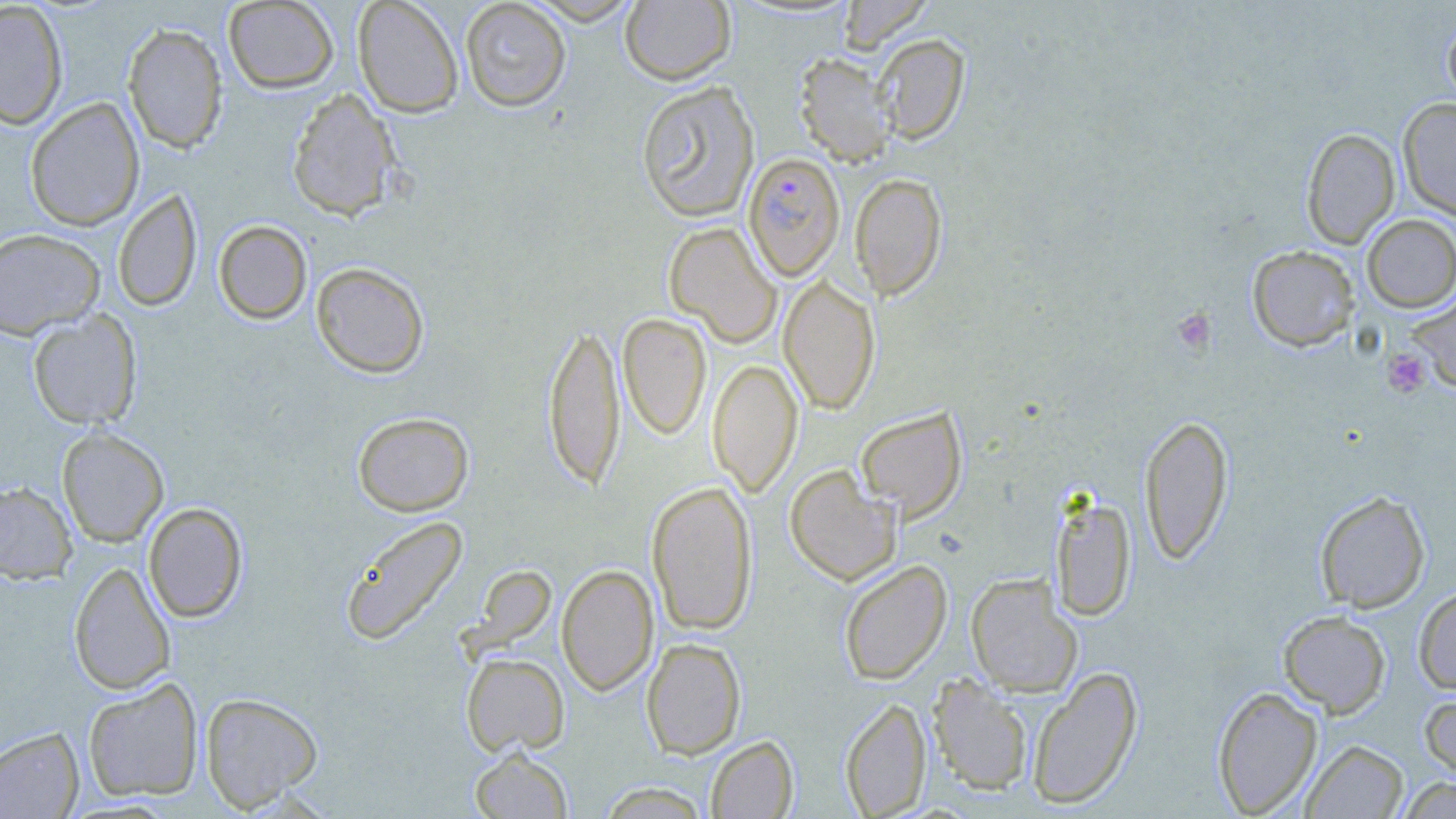

Summary:
  - Coordinate format: approximate bounding boxes as [x1, y1, x2, y2] in pixels
  - Uninfected red blood cell locations: [223, 0, 339, 93], [352, 0, 464, 118], [459, 0, 572, 112], [526, 0, 644, 25], [620, 0, 736, 85], [837, 0, 933, 55], [0, 2, 69, 130], [1442, 13, 1456, 112], [122, 22, 228, 154], [873, 33, 969, 143], [793, 53, 896, 166], [636, 80, 761, 222], [286, 88, 401, 221], [25, 97, 145, 231], [1398, 98, 1456, 220], [1301, 128, 1400, 248], [850, 173, 947, 300], [112, 189, 202, 312], [1361, 214, 1456, 312], [214, 220, 312, 324], [664, 222, 781, 347], [0, 228, 105, 339], [1246, 245, 1359, 351], [311, 262, 430, 378], [779, 274, 880, 414], [1405, 291, 1456, 393], [27, 310, 143, 429], [618, 313, 712, 440], [543, 319, 625, 491], [708, 358, 803, 497], [855, 407, 967, 521], [352, 411, 474, 516], [1138, 414, 1235, 565], [57, 427, 169, 547], [784, 465, 901, 585], [646, 480, 758, 635], [0, 481, 77, 583], [1314, 489, 1431, 613], [1050, 493, 1137, 622], [143, 502, 248, 623], [339, 514, 469, 646], [837, 560, 952, 684], [69, 561, 175, 695], [556, 564, 658, 696], [966, 573, 1081, 696], [1413, 585, 1456, 695], [1278, 610, 1391, 717], [641, 637, 747, 759], [461, 653, 569, 757], [1026, 666, 1143, 809], [927, 673, 1034, 796], [83, 678, 203, 802], [1212, 685, 1323, 817], [1419, 690, 1456, 786], [200, 692, 322, 812], [839, 697, 931, 818], [0, 727, 84, 818], [705, 735, 799, 818], [1301, 739, 1409, 818], [469, 746, 573, 818], [1396, 777, 1456, 818], [596, 782, 713, 818]
  - Platelet locations: [1172, 307, 1216, 356], [1382, 348, 1431, 398]
  - Plasmodium falciparum-infected red blood cell locations: [743, 152, 845, 281]
  - Slide-level diagnosis: Plasmodium falciparum
  - Stain: May-Grünwald-Giemsa
  - Field of view: one of a larger specimen
  - Preparation: thin blood film
  - Magnification: 1000x
  - Image size: 1456×819 pixels
  - Modality: light microscopy